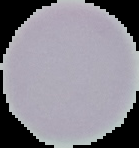
malaria status = uninfected
preparation = thin blood film
image size = 139×148 pixels
image type = segmented cell region with the area outside set to black